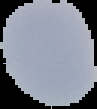

Summary:
  - Image type: cell region segmented out of the field of view; surrounding area masked to black
  - Result: no malaria parasites seen
  - Image size: 97×109 pixels
  - Preparation: thin blood smear